Point out each leukocyte.
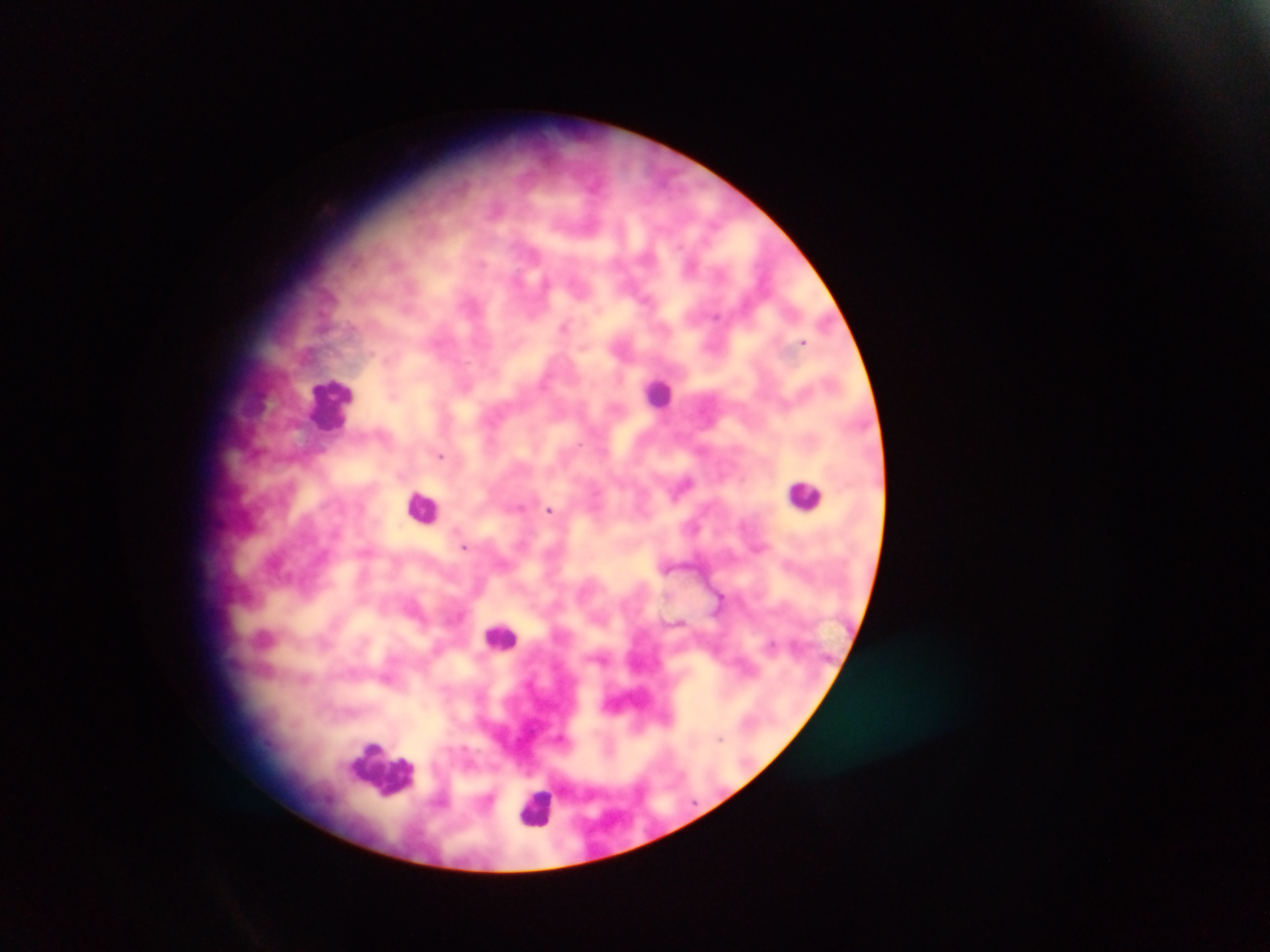

Approximate centers as (x, y) in pixels.
Leukocytes: (660, 392), (331, 402), (804, 495), (423, 507), (501, 636), (384, 769), (538, 804).

capture = mobile-phone photograph through a microscope
image size = 1270×952 pixels
preparation = thick blood smear
country = Ghana
field of view = single
malaria parasite locations = approximate centers as (x, y) in pixels: (716, 316), (565, 326), (803, 342), (440, 456), (684, 484), (520, 507), (549, 510), (464, 546), (771, 644), (304, 678), (721, 739)